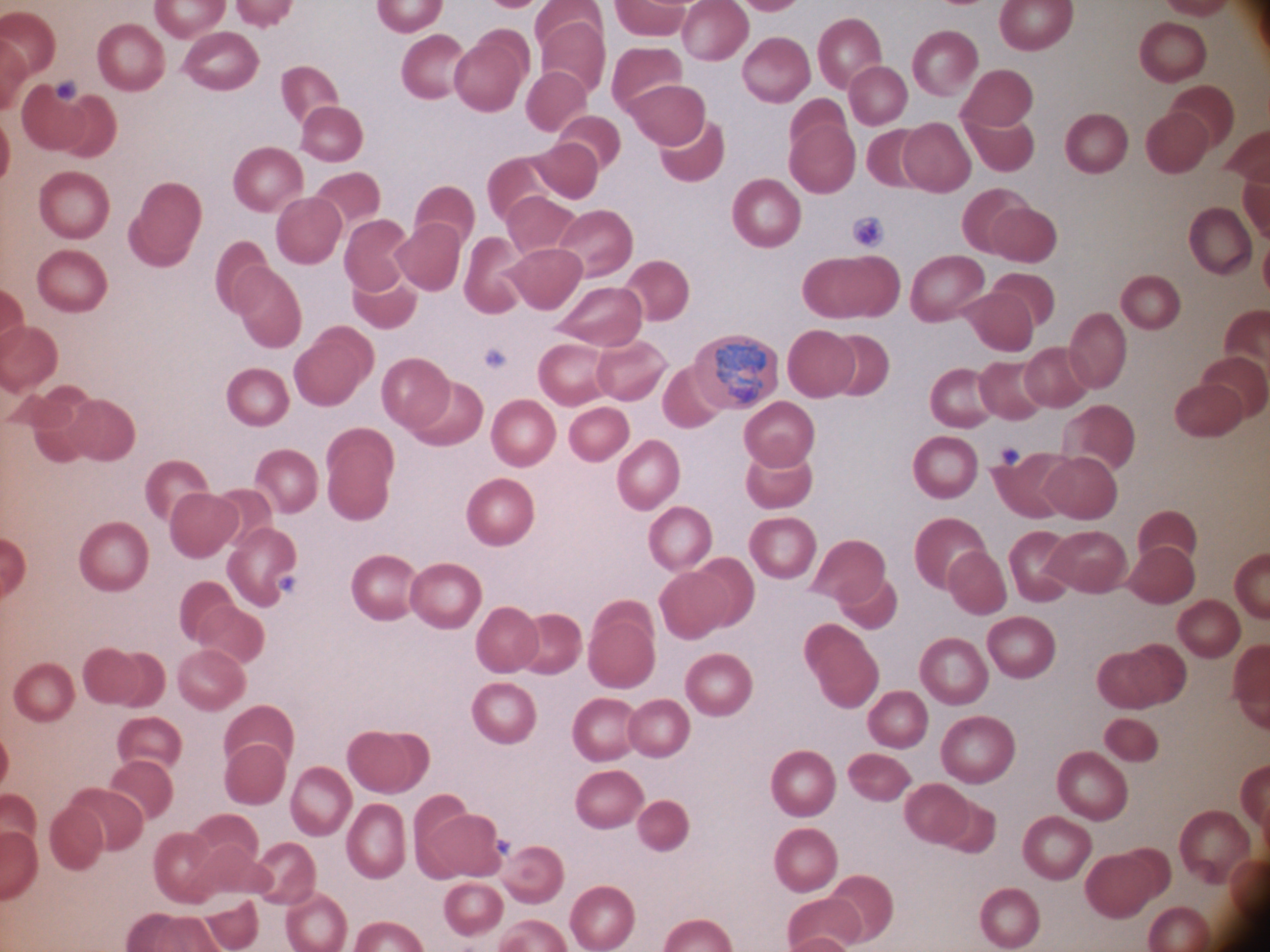
Approximate bounding boxes as (x1,y1)-(x2,y2) corner pairs in pixels, from the source annotation, which is not necessarily exhaustive. Trophozoite locations: (716,340)-(766,404). Species: Plasmodium ovale. Captured at 100x magnification. Image is 1270×952 pixels. Thin blood smear. One field from this slide. Giemsa stain. Leica DM2000 optical microscope with a built-in camera.